Locate every Plasmodium falciparum parasite and identify its life-cycle stage.
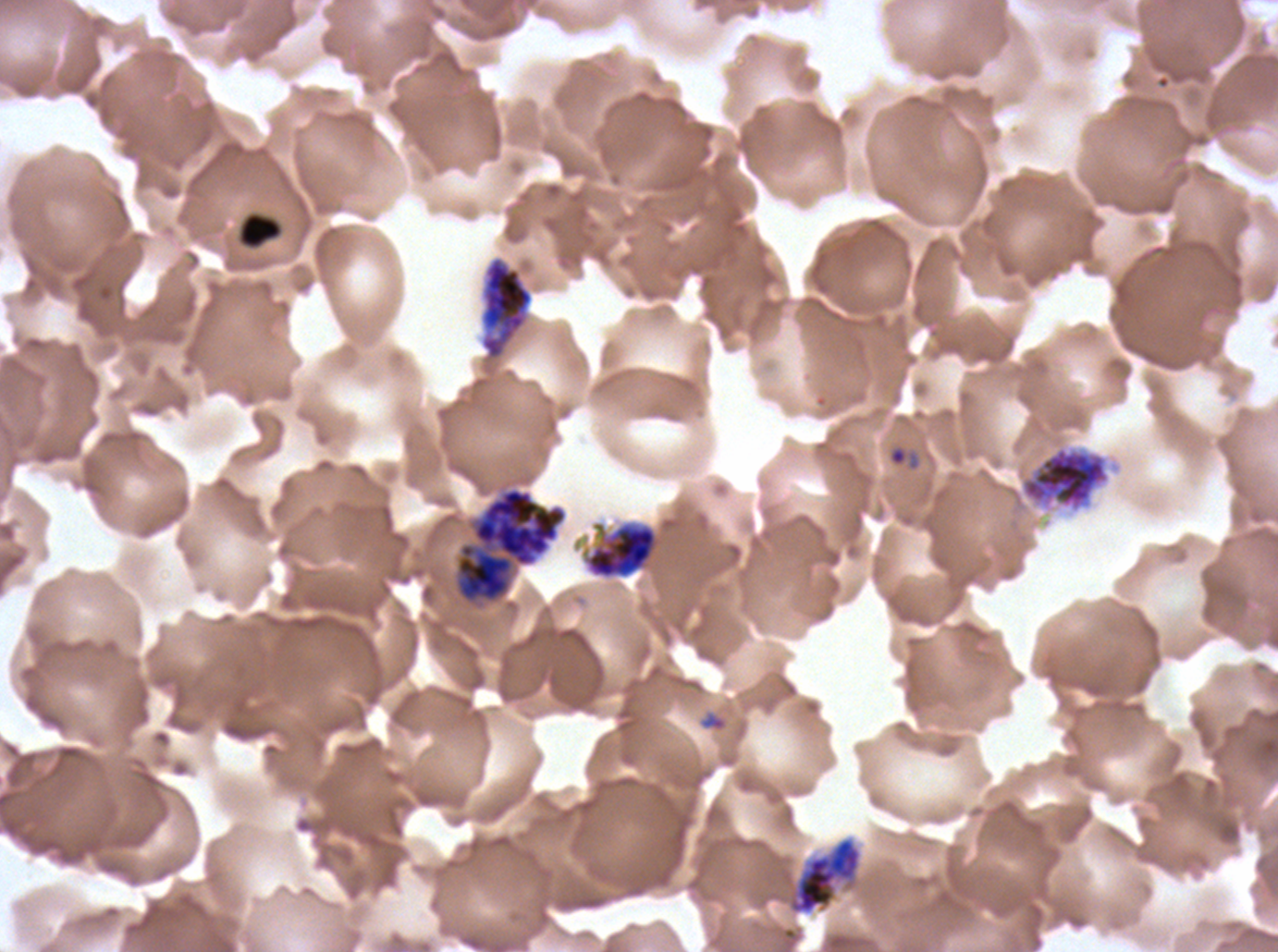

Approximate bounding boxes as {x1, y1, x2, y2} in pixels.
Rings: {887, 445, 921, 470}, {699, 712, 728, 732}.
Late-ring/early-trophozoite forms: {239, 213, 282, 249}.
Early schizonts: {480, 256, 534, 360}, {1019, 445, 1111, 512}, {585, 522, 657, 579}.
Late schizonts: {787, 836, 863, 915}.
Segmenters: {453, 486, 568, 606}.
No mid trophozoites, late trophozoites, or gametocytes observed.

preparation = thin blood film
field of view = one sub-image of a larger composite
specimen = Plasmodium falciparum from a patient in The Gambia, cultured ex vivo for 24 to 48 hours
stain = Giemsa
image size = 1278×952 pixels
life-cycle stages observed = ring, late-ring/early-trophozoite, early schizont, late schizont, segmenter